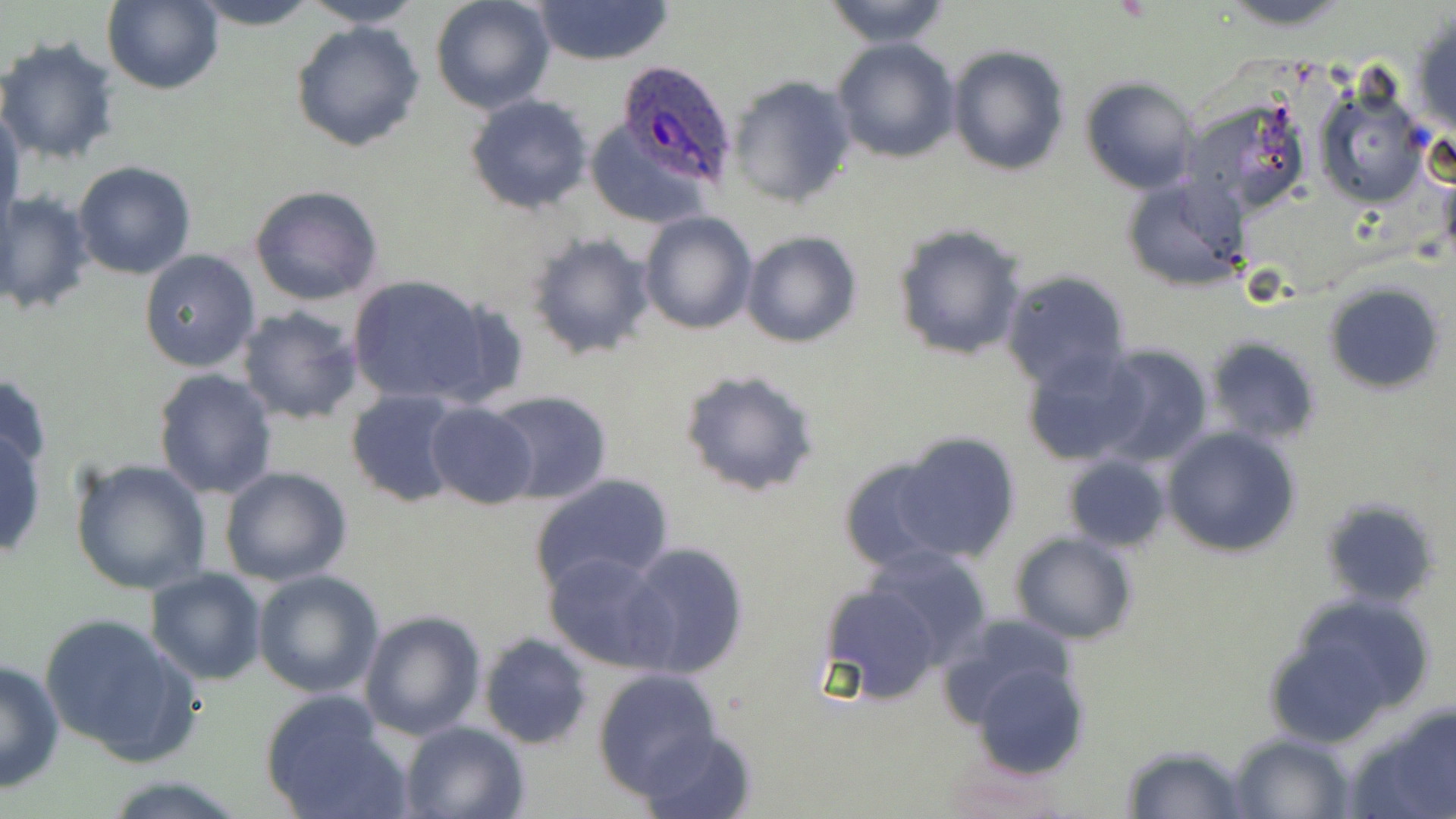
slide_level_diagnosis: Plasmodium ovale
preparation: thin blood film
uninfected_red_blood_cell_locations: 'approximate bounding boxes as (x1, y1, x2, y2) in pixels: (184, 0, 326, 29), (297, 0, 426, 29), (430, 0, 557, 115), (530, 0, 676, 67), (820, 0, 955, 47), (1214, 0, 1360, 29), (101, 2, 223, 93), (1409, 11, 1456, 139), (289, 20, 426, 153), (0, 34, 122, 168), (831, 36, 960, 165), (945, 44, 1071, 177), (724, 74, 856, 210), (1080, 77, 1201, 195), (1313, 85, 1430, 209), (463, 93, 594, 214), (1187, 96, 1313, 221), (1, 107, 24, 231), (586, 119, 715, 228), (72, 160, 197, 281), (1439, 169, 1456, 270), (1120, 174, 1248, 293), (248, 184, 383, 307), (0, 189, 96, 315), (639, 211, 758, 334), (893, 224, 1029, 361), (742, 231, 862, 349), (525, 232, 655, 360), (138, 249, 262, 373), (1000, 269, 1133, 393), (347, 273, 496, 408), (1324, 281, 1447, 394), (235, 305, 364, 426), (1203, 337, 1322, 445), (1090, 345, 1215, 467), (1022, 349, 1152, 468), (677, 368, 822, 498), (152, 369, 277, 501), (0, 370, 52, 483), (345, 388, 471, 508), (484, 389, 614, 504), (426, 402, 539, 511), (0, 415, 49, 558), (1162, 426, 1301, 557), (894, 431, 1021, 564), (836, 452, 970, 573), (1060, 452, 1170, 554), (68, 457, 212, 596), (218, 465, 353, 587), (530, 474, 673, 596), (1319, 499, 1440, 609), (1010, 531, 1137, 644), (619, 542, 749, 681), (860, 544, 995, 671), (545, 552, 673, 671), (145, 567, 267, 684), (252, 570, 383, 699), (818, 581, 947, 707), (1266, 592, 1439, 742), (359, 610, 486, 741), (38, 611, 200, 767), (935, 612, 1081, 730), (478, 632, 593, 750), (0, 657, 65, 795), (970, 660, 1090, 777), (592, 669, 721, 798), (258, 691, 409, 819), (1350, 702, 1456, 819), (399, 720, 529, 818), (638, 728, 760, 819), (1227, 731, 1355, 817), (1121, 745, 1249, 818), (105, 777, 246, 817)'
image_size: 1456×819 pixels
modality: light microscopy
stain: May-Grünwald-Giemsa
plasmodium_ovale_infected_red_blood_cell_locations: 'approximate bounding boxes as (x1, y1, x2, y2) in pixels: (612, 58, 739, 192)'
field_of_view: one of a larger specimen
magnification: 1000x